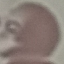

malaria_status: parasitized
stain: Giemsa
preparation: thin blood smear
image_type: cell patch, automatically extracted from a larger field of view and resized to 64 × 64 pixels
capture: smartphone through the microscope eyepiece